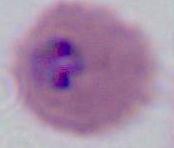
modality: micrograph
identification: Plasmodium
magnification: 400x or 1000x